Comment on the morphology of the erythrocytes.
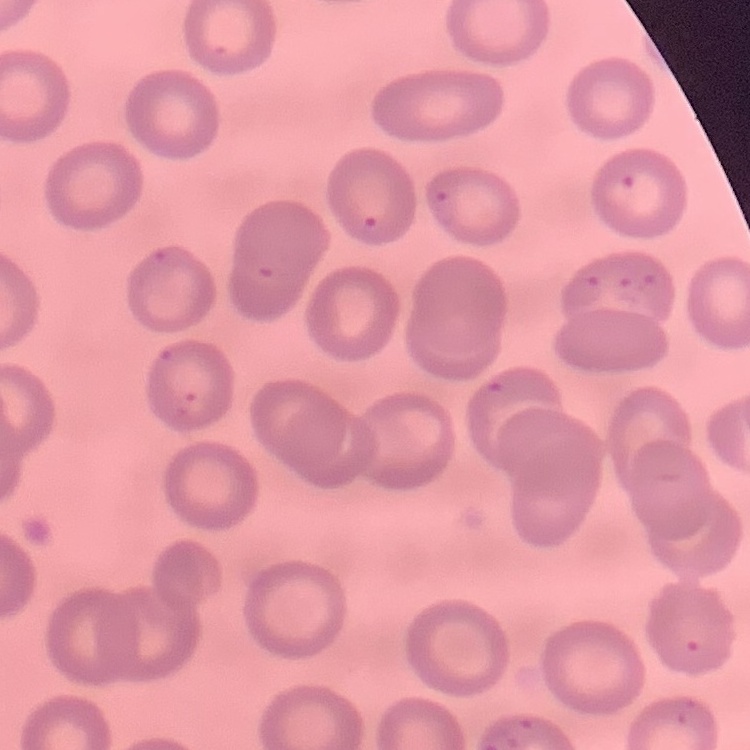
No rouleaux formation.

Thin blood film. Stained with either Field's or Giemsa. Square crop of a larger photomicrograph.